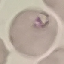
Summary:
  - Result: malaria parasites detected
  - Image type: cell patch, automatically extracted from a larger field of view and resized to 64 × 64 pixels
  - Preparation: thin blood smear
  - Capture: smartphone camera at the microscope eyepiece
  - Stain: Giemsa